Report the malaria status of this cell.
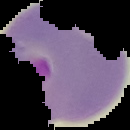

Parasitized.

{
  "preparation": "thin blood smear",
  "image_type": "segmented cell region on a black background",
  "image_size": "130×130 pixels"
}